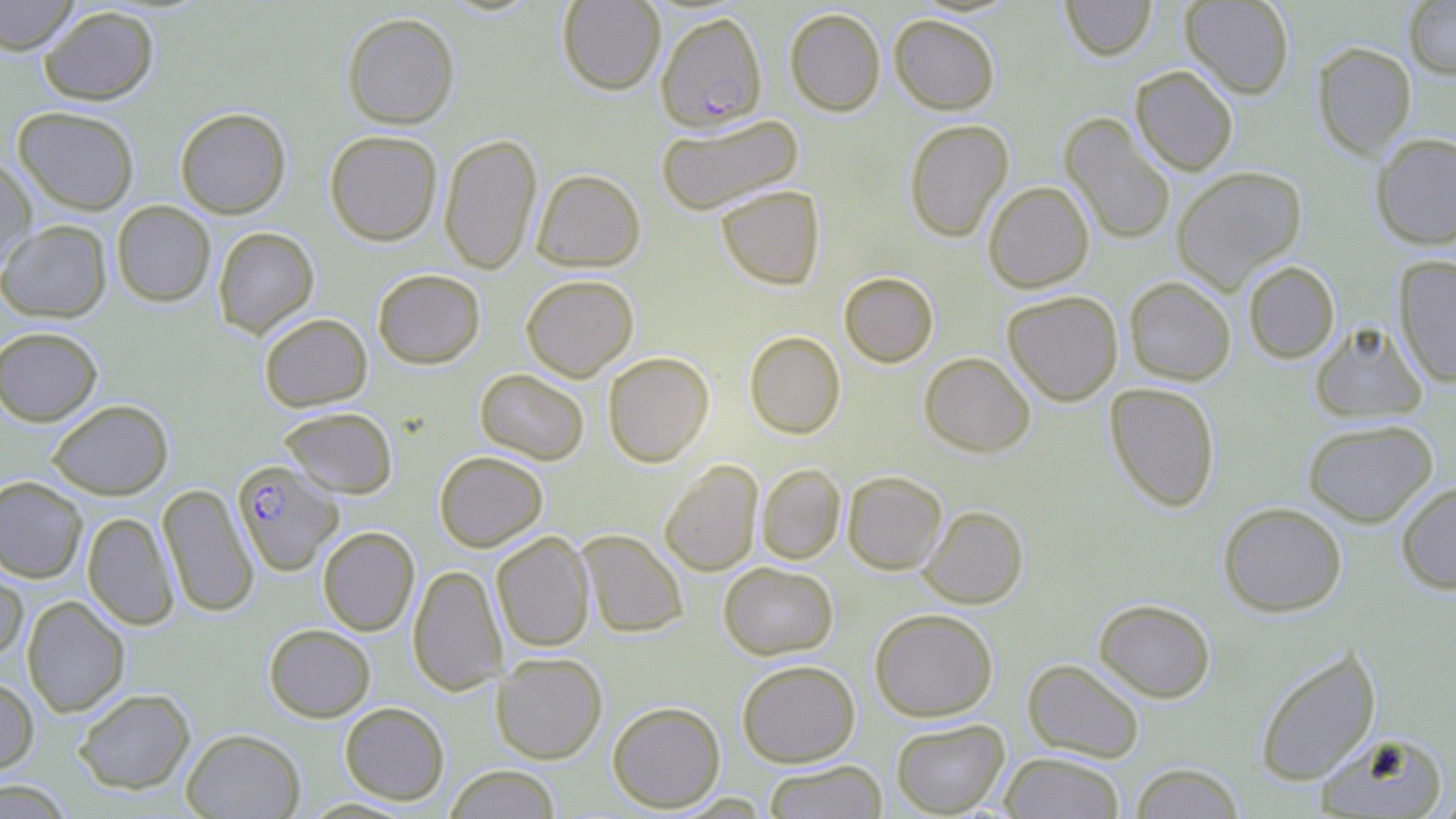
Summary:
  - Coordinate format: approximate bounding boxes as (x1, y1, x2, y2) in pixels
  - Plasmodium falciparum-infected red blood cell locations: (655, 11, 767, 132), (232, 459, 342, 575)
  - Uninfected red blood cell locations: (0, 0, 79, 55), (556, 0, 666, 95), (1060, 0, 1157, 61), (1181, 0, 1294, 99), (1403, 0, 1456, 79), (39, 5, 159, 105), (784, 7, 886, 116), (342, 12, 459, 129), (889, 13, 1000, 115), (1312, 42, 1416, 159), (1130, 65, 1238, 176), (13, 106, 140, 215), (174, 107, 291, 219), (655, 113, 805, 216), (1060, 114, 1175, 246), (903, 119, 1014, 242), (324, 130, 443, 246), (1371, 132, 1456, 249), (438, 133, 543, 274), (0, 156, 37, 272), (1171, 166, 1307, 292), (531, 168, 646, 271), (983, 181, 1094, 293), (716, 185, 825, 290), (111, 201, 216, 306), (0, 219, 112, 322), (213, 226, 319, 338), (1393, 256, 1456, 387), (1242, 260, 1340, 363), (372, 268, 485, 369), (839, 272, 938, 367), (521, 274, 639, 380), (1124, 276, 1236, 385), (1002, 290, 1123, 405), (259, 313, 372, 411), (1309, 321, 1428, 425), (0, 326, 102, 426), (744, 331, 846, 438), (602, 351, 714, 467), (919, 352, 1035, 456), (475, 368, 589, 465), (1104, 383, 1220, 512), (47, 399, 173, 499), (280, 406, 398, 498), (1302, 419, 1438, 527), (434, 451, 549, 551), (659, 461, 763, 576), (757, 463, 846, 565), (842, 470, 948, 574), (0, 476, 88, 583), (1395, 479, 1456, 594), (158, 484, 258, 617), (1218, 501, 1347, 617), (918, 505, 1028, 608), (82, 512, 180, 630), (317, 526, 419, 636), (578, 529, 689, 638), (492, 531, 595, 651), (0, 557, 29, 665), (718, 562, 838, 660), (726, 562, 842, 765), (408, 564, 507, 696), (22, 596, 130, 717), (1094, 598, 1216, 702), (869, 608, 998, 722), (264, 624, 375, 722), (1254, 644, 1383, 786), (492, 652, 607, 763), (737, 659, 860, 767), (1022, 659, 1145, 762), (0, 676, 39, 775), (73, 688, 195, 794), (339, 701, 450, 805), (607, 701, 725, 812), (890, 719, 1010, 817), (181, 728, 305, 818), (1314, 731, 1450, 818), (999, 751, 1125, 818), (763, 759, 888, 818), (1129, 762, 1246, 818), (444, 764, 561, 819), (0, 779, 73, 818), (1431, 790, 1456, 818), (297, 797, 421, 818)
  - Slide-level diagnosis: Plasmodium falciparum
  - Image size: 1456×819 pixels
  - Stain: May-Grünwald-Giemsa
  - Preparation: thin blood smear
  - Modality: light microscopy
  - Magnification: 1000x
  - Field of view: single